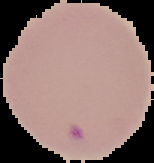 Image is 154×163 pixels. Result: negative for malaria parasites. From a thin blood smear. The area outside the segmented cell region is set to black.